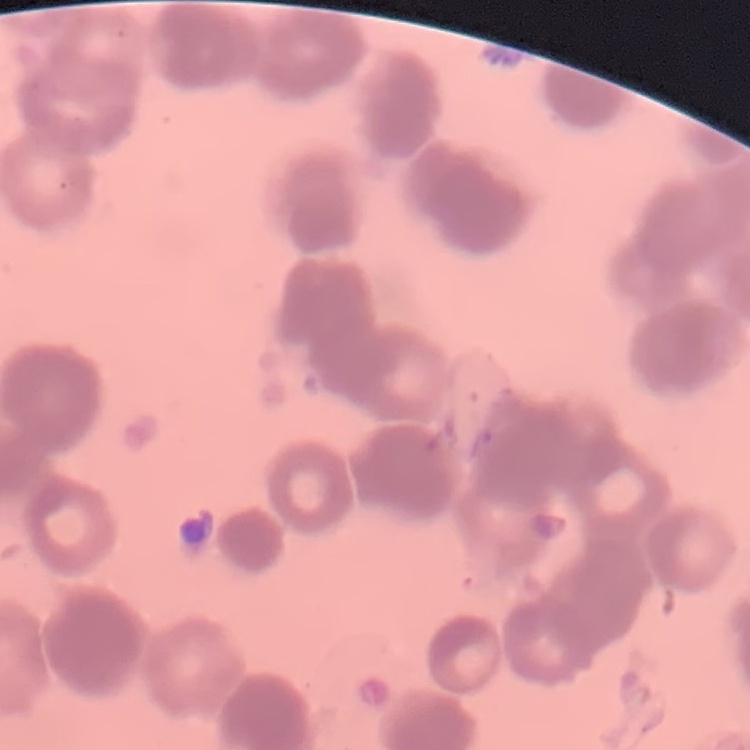

Summary:
  - Red blood cell morphology: rouleaux formation
  - Image type: one tile cut from a larger photomicrograph
  - Stain: Field's or Giemsa
  - Preparation: thin blood smear